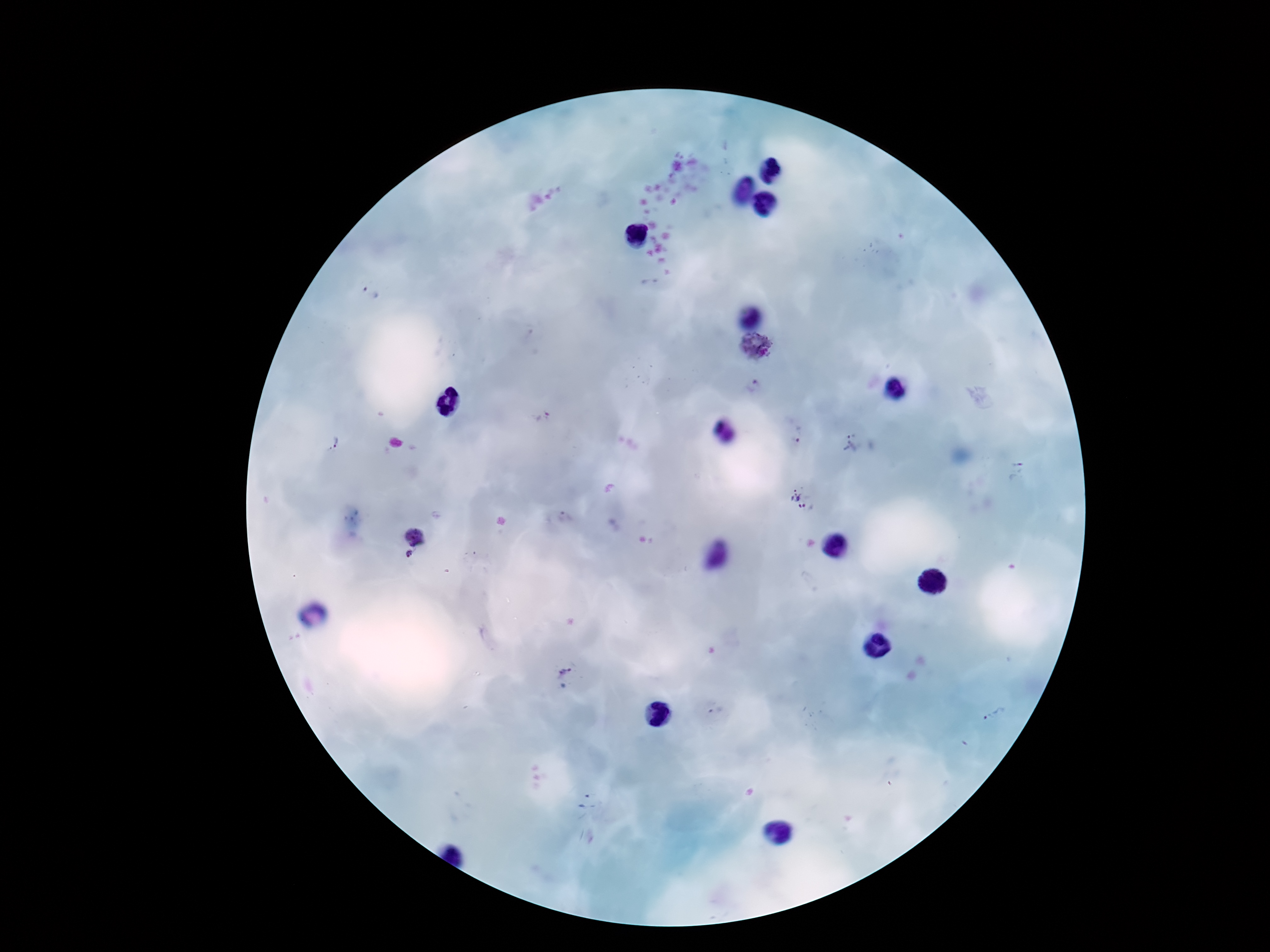
Approximate centers as (x, y) in pixels.
Summary:
  - Plasmodium parasite locations: (370, 293), (755, 346), (755, 386), (542, 416), (798, 434), (334, 441), (850, 445), (798, 498), (566, 517), (417, 535), (409, 553), (564, 668), (715, 712), (994, 718)
  - Field of view: one from this slide
  - Preparation: thick blood film
  - Capture: smartphone camera through the microscope eyepiece
  - Stain: Giemsa
  - Magnification: 100x
  - Image size: 1270×952 pixels
  - Patient malaria status: infected